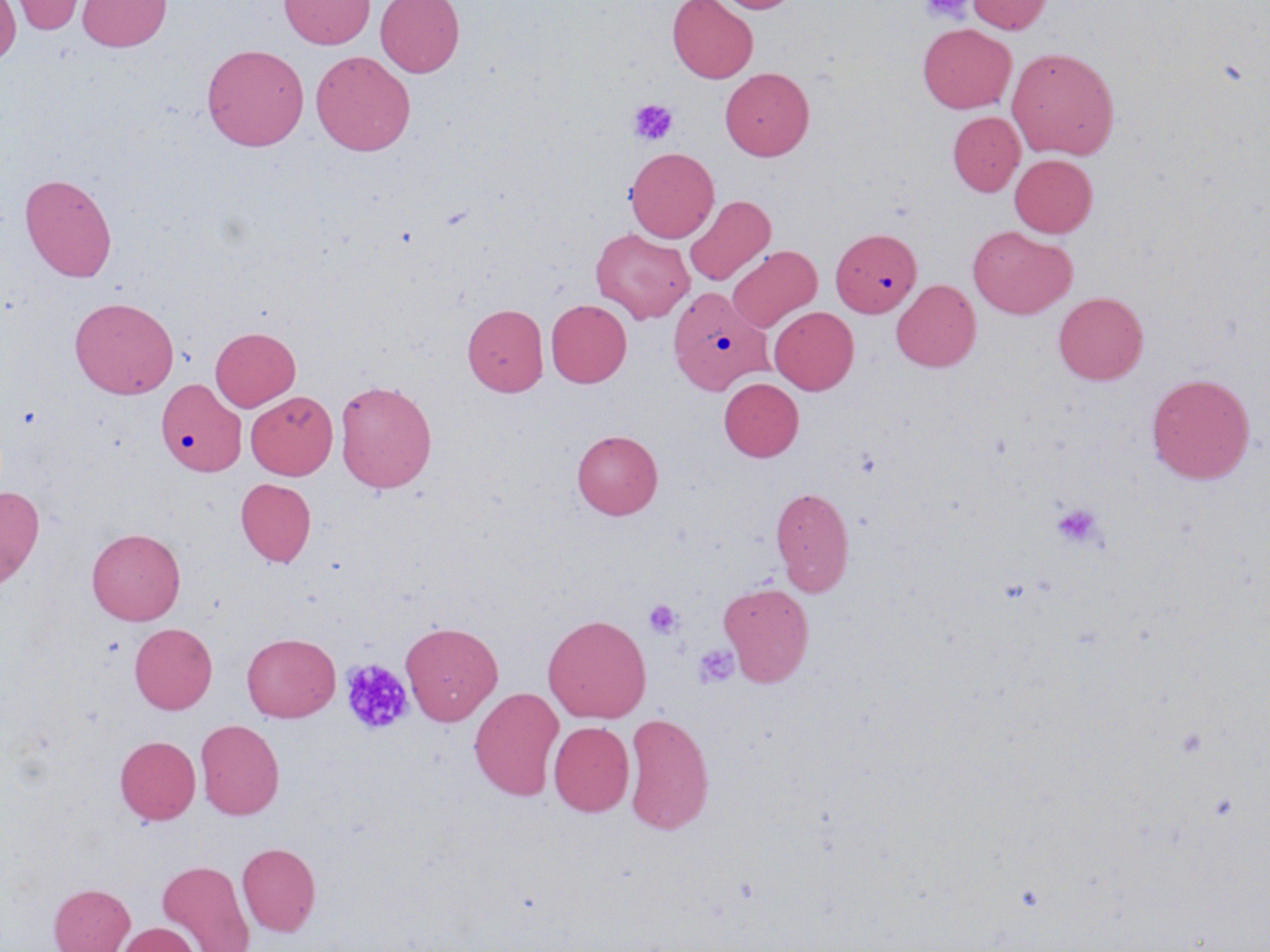
slide_level_diagnosis: no evidence of blood parasites
image_size: 1270×952 pixels
uninfected_red_blood_cell_locations: 'approximate bounding boxes as [x1, y1, x2, y2] in pixels: [7, 0, 88, 35], [77, 0, 171, 52], [279, 0, 374, 49], [375, 0, 464, 77], [667, 0, 758, 83], [713, 0, 799, 13], [966, 0, 1053, 34], [0, 1, 21, 65], [917, 23, 1016, 113], [201, 43, 309, 151], [1006, 47, 1120, 160], [310, 50, 416, 156], [720, 68, 814, 160], [948, 112, 1024, 196], [625, 147, 719, 242], [1010, 154, 1097, 237], [19, 172, 117, 281], [683, 195, 775, 286], [968, 226, 1076, 319], [831, 227, 921, 318], [590, 228, 695, 324], [727, 245, 821, 332], [891, 279, 981, 372], [668, 287, 770, 396], [1054, 292, 1148, 385], [69, 296, 179, 399], [546, 299, 631, 388], [462, 304, 548, 396], [769, 306, 858, 394], [210, 326, 300, 411], [1147, 373, 1255, 483], [719, 377, 803, 461], [158, 380, 247, 478], [334, 380, 437, 493], [246, 391, 338, 479], [571, 429, 663, 519], [235, 478, 316, 567], [0, 485, 45, 588], [770, 486, 855, 595], [86, 527, 186, 625], [718, 582, 815, 686], [543, 614, 651, 723], [401, 621, 503, 724], [129, 623, 217, 714], [241, 633, 340, 722], [469, 687, 564, 800], [623, 712, 714, 835], [195, 719, 284, 820], [548, 720, 634, 817], [115, 735, 201, 824], [237, 842, 321, 936], [157, 860, 254, 952], [49, 883, 134, 952], [116, 922, 200, 952]'
stain: May-Grünwald-Giemsa
modality: optical microscopy
field_of_view: one of a larger specimen
preparation: thin blood smear
magnification: 1000x
platelet_locations: 'approximate bounding boxes as [x1, y1, x2, y2] in pixels: [920, 0, 973, 23], [628, 99, 678, 145], [1051, 502, 1105, 549], [643, 599, 684, 639], [692, 643, 740, 690], [339, 658, 413, 734], [1175, 725, 1209, 757]'